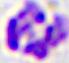

Summary:
  - Magnification: 400x
  - Modality: micrograph
  - Identification: leukocyte